Classify this cell by malaria status.
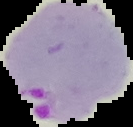

Parasitized.

From a thin blood smear. Segmented cell region on a black background. Image is 133×127 pixels.